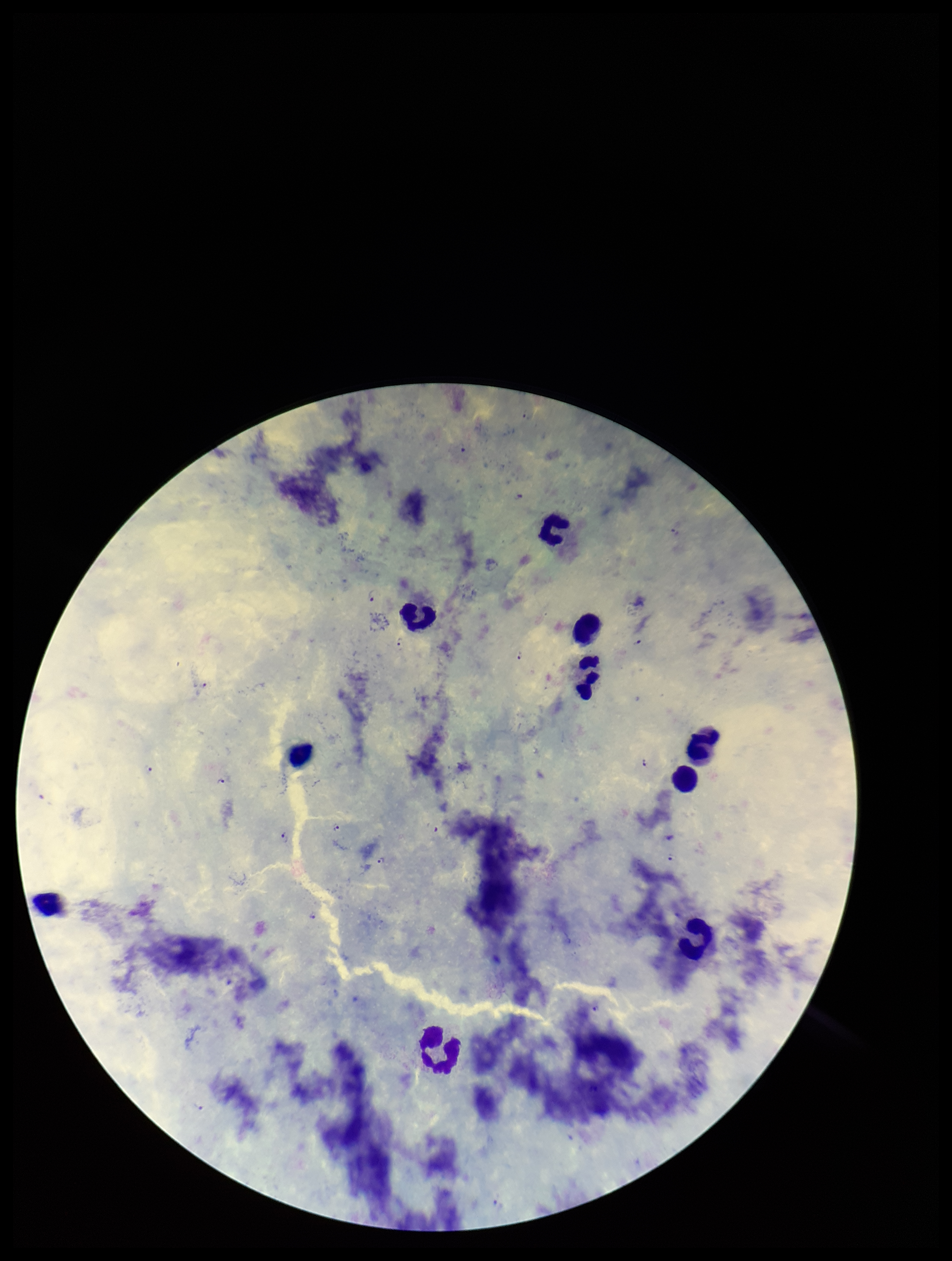
image_size: 952×1261 pixels
preparation: thick smear
species_reported_for_this_patient: Plasmodium falciparum
field_of_view: single
patient_malaria_status: infected
leukocyte_count: 10
stain: Giemsa
parasite_count: 12
capture: smartphone photograph through the microscope eyepiece
plasmodium_parasites: detected